Report the malaria status of this cell.
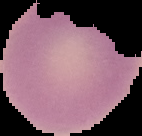
Uninfected.

image type = segmented cell region with the area outside set to black
image size = 142×136 pixels
preparation = thin blood film